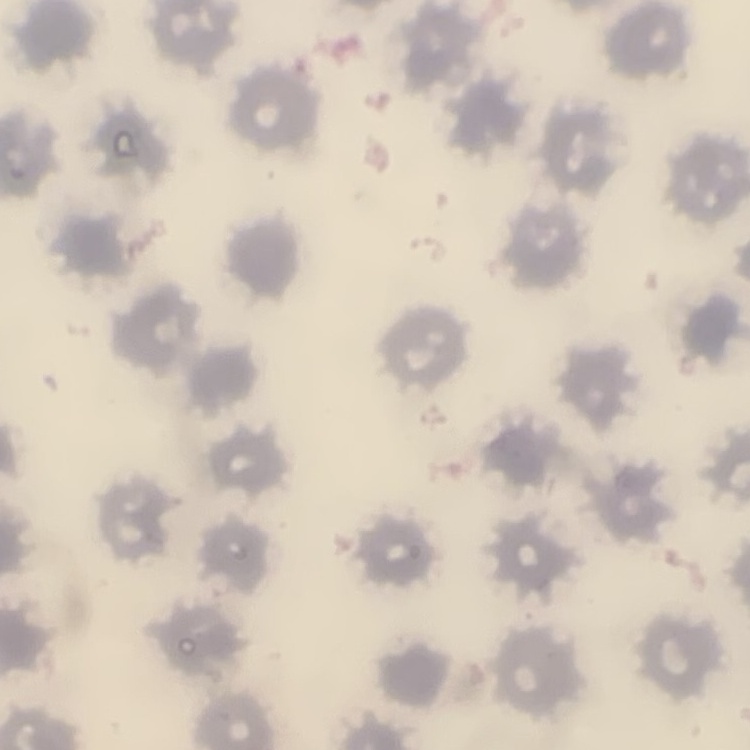
{
  "erythrocyte_morphology": "no rouleaux formation",
  "stain": "Field's or Giemsa",
  "image_type": "square crop of a larger photomicrograph",
  "preparation": "thin blood smear"
}